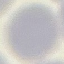
Summary:
  - Result: no malaria parasites detected
  - Stain: Giemsa
  - Preparation: thin blood smear
  - Capture: smartphone through the microscope eyepiece
  - Image type: cell patch, automatically extracted from a larger field of view and resized to 64 × 64 pixels